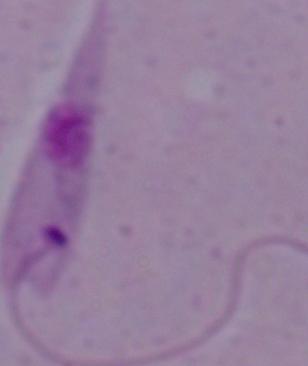 Photomicrograph. A Leishmania parasite is shown. 1000x magnification.